Identify the cell.
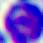
A leukocyte.

Summary:
  - Magnification: 400x
  - Modality: micrograph